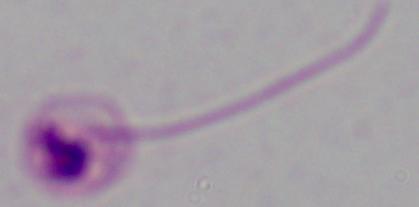
magnification = 1000x
identification = Leishmania
modality = micrograph